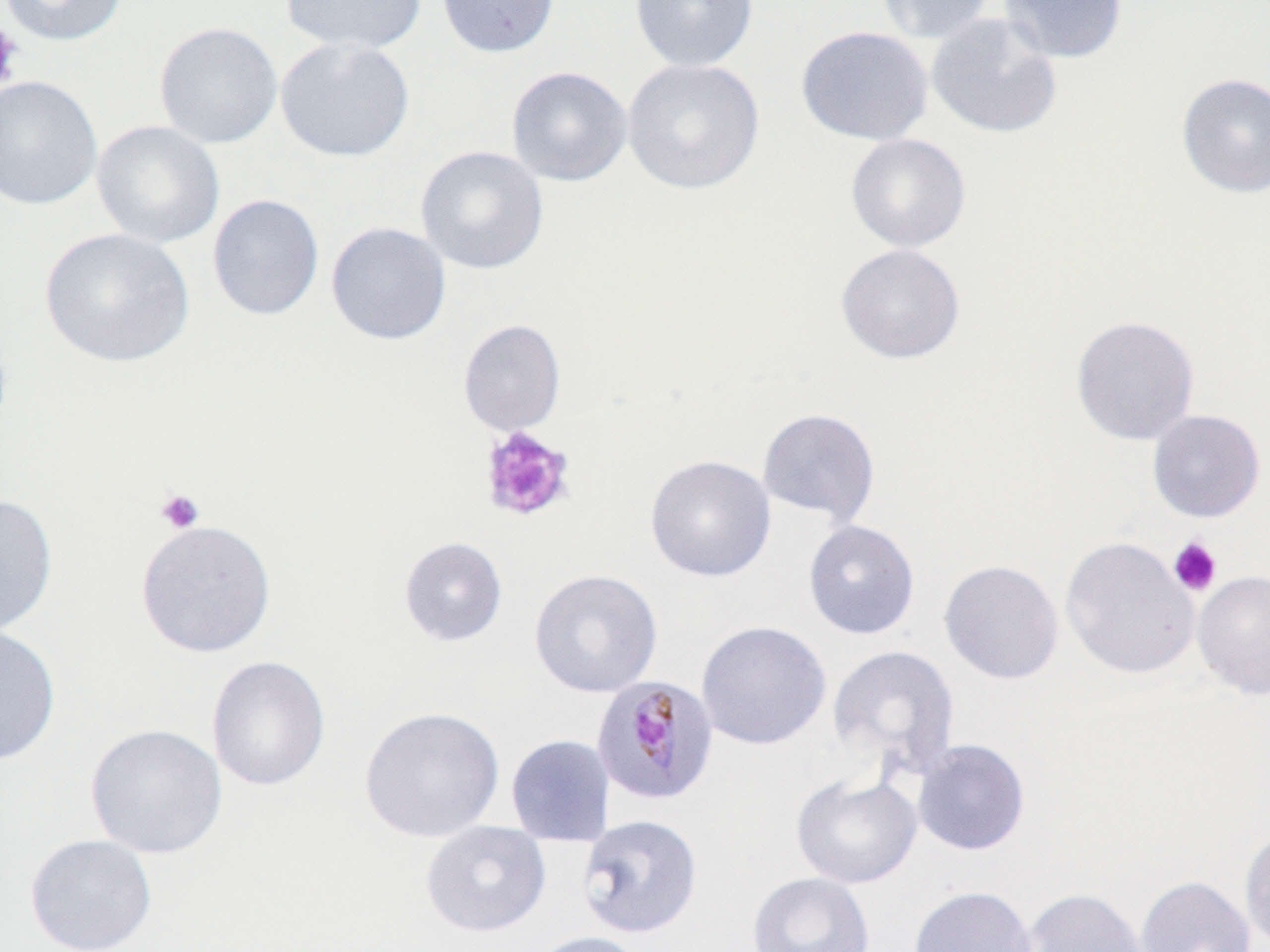

slide-level diagnosis = Plasmodium malariae
magnification = 1000x
platelet locations = approximate bounding boxes as (x1, y1, x2, y2) in pixels: (0, 21, 23, 92), (478, 426, 576, 523), (155, 488, 205, 534), (1168, 537, 1223, 597)
preparation = thin blood film
uninfected red blood cell locations = approximate bounding boxes as (x1, y1, x2, y2) in pixels: (0, 0, 127, 46), (279, 0, 427, 54), (436, 0, 560, 58), (630, 0, 759, 72), (877, 0, 996, 45), (999, 0, 1129, 64), (925, 12, 1063, 139), (154, 21, 283, 149), (795, 25, 933, 146), (274, 37, 415, 162), (622, 58, 765, 195), (506, 66, 632, 187), (1176, 73, 1270, 198), (0, 75, 103, 210), (91, 120, 225, 249), (845, 133, 971, 253), (415, 145, 549, 274), (207, 194, 324, 321), (325, 221, 451, 345), (40, 228, 195, 368), (835, 243, 966, 364), (1070, 314, 1200, 445), (458, 319, 566, 436), (756, 407, 880, 526), (1146, 409, 1266, 522), (645, 454, 777, 582), (0, 493, 58, 638), (135, 519, 277, 658), (802, 520, 920, 640), (398, 536, 508, 646), (1060, 536, 1200, 680), (939, 559, 1065, 684), (529, 568, 663, 698), (1192, 570, 1270, 699), (696, 620, 832, 751), (0, 625, 62, 766), (827, 645, 960, 779), (207, 655, 331, 791), (359, 706, 505, 843), (85, 723, 227, 859), (505, 734, 615, 847), (912, 739, 1030, 856), (791, 772, 922, 889), (577, 813, 703, 939), (419, 820, 551, 937), (1239, 826, 1270, 950), (25, 833, 158, 952), (746, 871, 876, 952), (1135, 876, 1256, 952), (908, 885, 1039, 952), (1021, 887, 1150, 952), (526, 930, 650, 952)
modality = light microscopy
Plasmodium malariae-infected red blood cell locations = approximate bounding boxes as (x1, y1, x2, y2) in pixels: (590, 674, 720, 807)
image size = 1270×952 pixels
stain = May-Grünwald-Giemsa
field of view = single